Assess this cell for malaria.
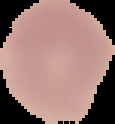

It is uninfected.

Image is 115×124 pixels. The area outside the segmented cell region is set to black. From a thin blood smear.